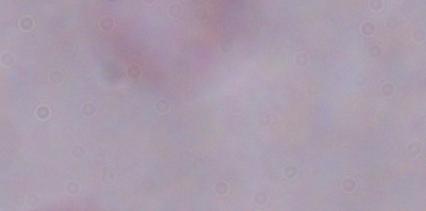

Summary:
  - Modality: micrograph
  - Magnification: 1000x
  - Identification: trypanosome